State the blood parasite species.
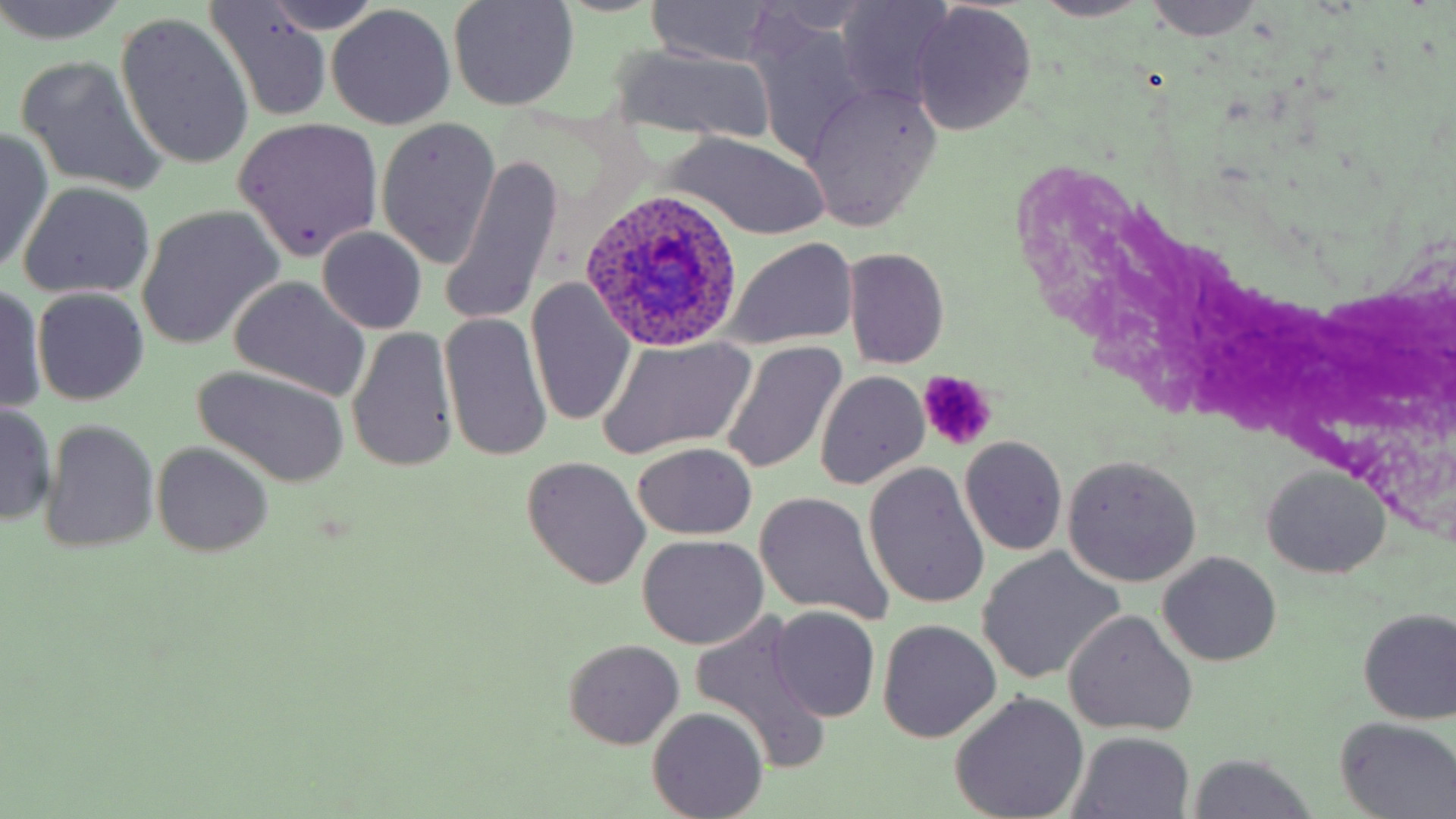
Plasmodium ovale.

magnification = 1000x
Plasmodium ovale-infected red blood cell locations = approximate bounding boxes as (x1,y1)-(x2,y2) corner pairs in pixels: (579,189)-(742,352)
field of view = single
image size = 1456×819 pixels
uninfected red blood cell locations = approximate bounding boxes as (x1,y1)-(x2,y2) corner pairs in pixels: (0,0)-(131,47), (447,0)-(579,111), (1031,0)-(1153,22), (1143,0)-(1261,40), (647,1)-(780,68), (834,1)-(960,108), (206,4)-(334,118), (908,5)-(1036,133), (325,7)-(455,129), (116,15)-(254,170), (607,43)-(779,147), (16,55)-(166,193), (803,85)-(942,229), (232,117)-(383,262), (376,118)-(501,268), (0,130)-(53,274), (664,133)-(831,239), (440,153)-(562,327), (18,182)-(155,300), (138,207)-(282,346), (316,227)-(428,335), (724,238)-(858,349), (843,247)-(950,368), (228,277)-(371,400), (527,278)-(636,429), (0,281)-(47,414), (33,289)-(150,404), (438,311)-(553,463), (347,326)-(460,473), (595,337)-(756,460), (719,341)-(848,476), (189,367)-(350,488), (815,371)-(930,490), (1,400)-(57,526), (41,420)-(159,554), (959,436)-(1067,556), (153,442)-(273,556), (632,442)-(757,539), (1063,455)-(1203,586), (521,459)-(651,590), (864,462)-(990,610), (1260,466)-(1391,580), (755,492)-(892,623), (636,534)-(770,650), (977,549)-(1124,683), (1159,552)-(1281,667), (768,606)-(880,723), (1358,608)-(1456,725), (1064,612)-(1197,737), (691,615)-(832,771), (878,620)-(1002,742), (562,639)-(685,749), (951,693)-(1088,819), (649,708)-(767,819), (1336,717)-(1455,819), (1070,734)-(1194,819), (1190,756)-(1314,819)
platelet locations = approximate bounding boxes as (x1,y1)-(x2,y2) corner pairs in pixels: (916,370)-(996,449)
modality = light microscopy
preparation = thin blood smear
stain = May-Grünwald-Giemsa